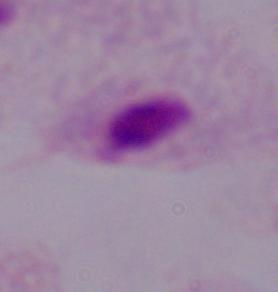

1000x magnification. Micrograph. A trichomonad is shown.